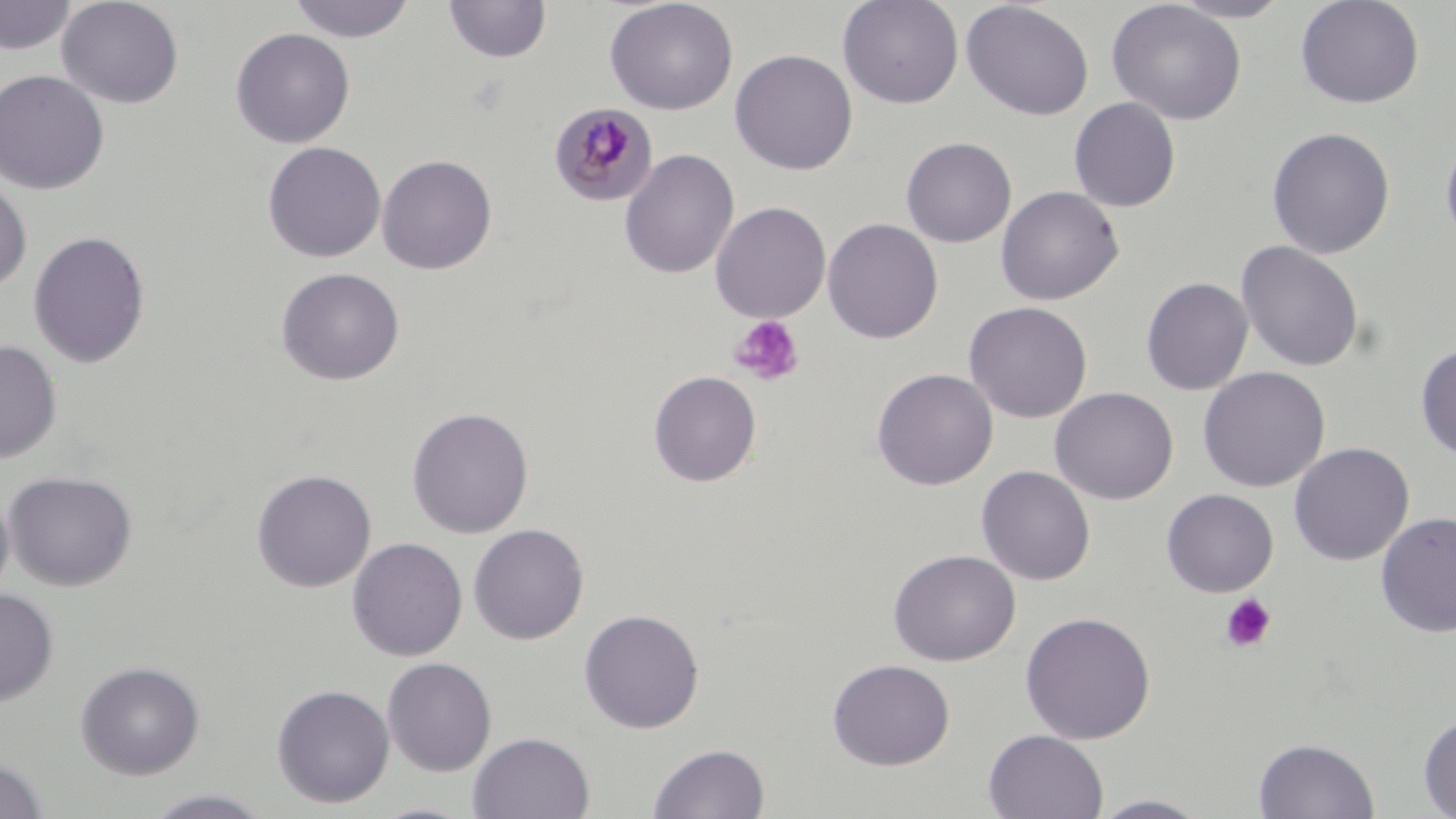

Approximate bounding boxes as [x1, y1, x2, y2] in pixels. Uninfected red blood cell locations: [56, 0, 185, 109], [287, 0, 417, 43], [605, 0, 738, 115], [837, 0, 964, 109], [1168, 0, 1292, 23], [1295, 0, 1425, 109], [0, 1, 77, 54], [442, 1, 552, 63], [960, 1, 1094, 121], [1107, 1, 1248, 125], [230, 27, 355, 148], [730, 49, 858, 175], [0, 69, 110, 195], [1068, 97, 1181, 212], [1266, 126, 1395, 259], [1440, 134, 1456, 255], [900, 136, 1017, 248], [262, 141, 386, 262], [619, 148, 739, 279], [376, 153, 497, 274], [0, 175, 33, 293], [995, 186, 1124, 305], [710, 201, 831, 323], [823, 218, 943, 344], [28, 230, 151, 368], [1236, 240, 1365, 372], [275, 266, 405, 385], [1141, 277, 1254, 395], [963, 301, 1093, 423], [0, 339, 62, 464], [1414, 342, 1456, 460], [1197, 366, 1330, 492], [872, 368, 998, 490], [648, 370, 762, 487], [1050, 387, 1178, 504], [406, 407, 534, 538], [1288, 442, 1414, 565], [976, 465, 1095, 586], [251, 469, 377, 593], [3, 470, 138, 591], [0, 488, 14, 605], [1161, 488, 1279, 597], [1375, 512, 1456, 638], [468, 523, 589, 644], [347, 537, 468, 661], [888, 549, 1021, 666], [0, 588, 59, 707], [579, 608, 705, 733], [1019, 611, 1157, 744], [381, 657, 497, 776], [827, 658, 955, 770], [75, 660, 205, 779], [271, 683, 395, 808], [1418, 710, 1456, 818], [983, 729, 1109, 818], [467, 731, 595, 819], [1253, 737, 1380, 819], [648, 742, 770, 819], [0, 758, 50, 818], [142, 788, 274, 818], [1088, 794, 1214, 818], [369, 802, 480, 818]. Platelet locations: [729, 315, 805, 387], [1219, 593, 1277, 653]. Plasmodium malariae-infected red blood cell locations: [548, 101, 659, 206]. Slide-level diagnosis: Plasmodium malariae. One field of a larger specimen. May-Grünwald-Giemsa stain. Captured at 1000x magnification. Light microscopy. Thin blood film. Image is 1456×819 pixels.